Name the parasite shown.
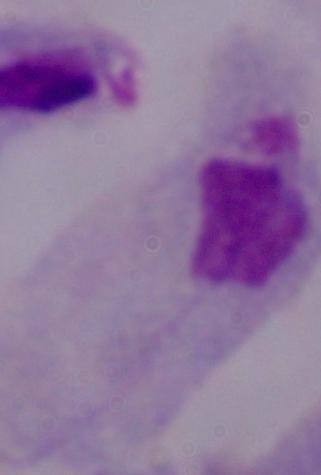
This is a trichomonad.

1000x magnification. Photomicrograph.